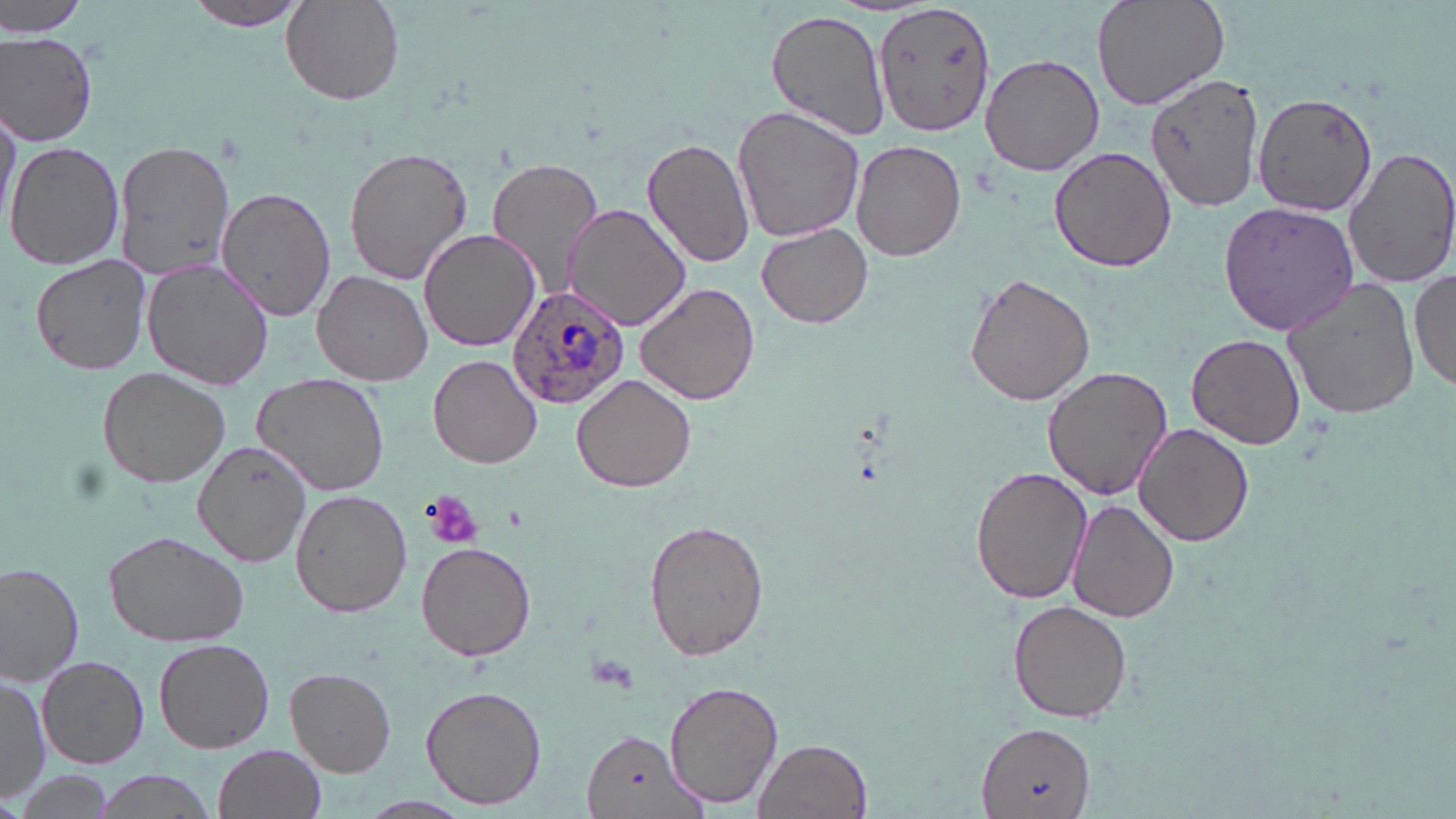 Approximate bounding boxes as (x1,y1)-(x2,y2) corner pairs in pixels. Uninfected red blood cell locations: (2,0)-(93,39), (181,0)-(312,32), (1090,0)-(1228,112), (281,2)-(405,106), (874,2)-(996,136), (766,8)-(891,139), (1,30)-(99,148), (980,54)-(1104,176), (1147,73)-(1264,212), (1252,91)-(1378,216), (0,100)-(20,238), (732,105)-(865,245), (111,138)-(236,282), (643,138)-(757,268), (6,139)-(127,270), (853,141)-(965,261), (1342,144)-(1456,290), (1050,145)-(1176,274), (344,147)-(474,284), (487,158)-(604,293), (217,185)-(339,322), (1217,201)-(1359,333), (562,203)-(693,332), (757,221)-(874,329), (420,228)-(540,352), (28,252)-(156,374), (143,261)-(272,390), (1411,268)-(1456,395), (312,269)-(433,386), (965,273)-(1095,407), (1281,276)-(1421,421), (637,282)-(761,405), (1187,331)-(1305,450), (428,353)-(543,468), (1043,365)-(1172,502), (97,367)-(229,489), (253,372)-(388,496), (572,374)-(695,494), (1134,423)-(1253,546), (192,441)-(311,569), (970,465)-(1092,605), (290,489)-(412,617), (1067,499)-(1178,622), (646,520)-(769,662), (101,530)-(250,646), (417,541)-(536,662), (0,562)-(84,685), (1009,600)-(1133,723), (152,637)-(274,753), (38,655)-(150,770), (285,667)-(396,777), (0,672)-(49,806), (663,680)-(782,809), (420,685)-(547,810), (975,723)-(1097,819), (582,729)-(704,818), (753,737)-(873,819), (212,744)-(327,819), (9,767)-(122,819), (89,771)-(221,819). Platelet locations: (423,490)-(485,549). Plasmodium ovale-infected red blood cell locations: (508,286)-(632,408). Slide-level diagnosis: Plasmodium ovale. Thin blood film. One field of a larger specimen. May-Grünwald-Giemsa-stained preparation. Captured at 1000x magnification. Light microscopy. Image is 1456×819 pixels.